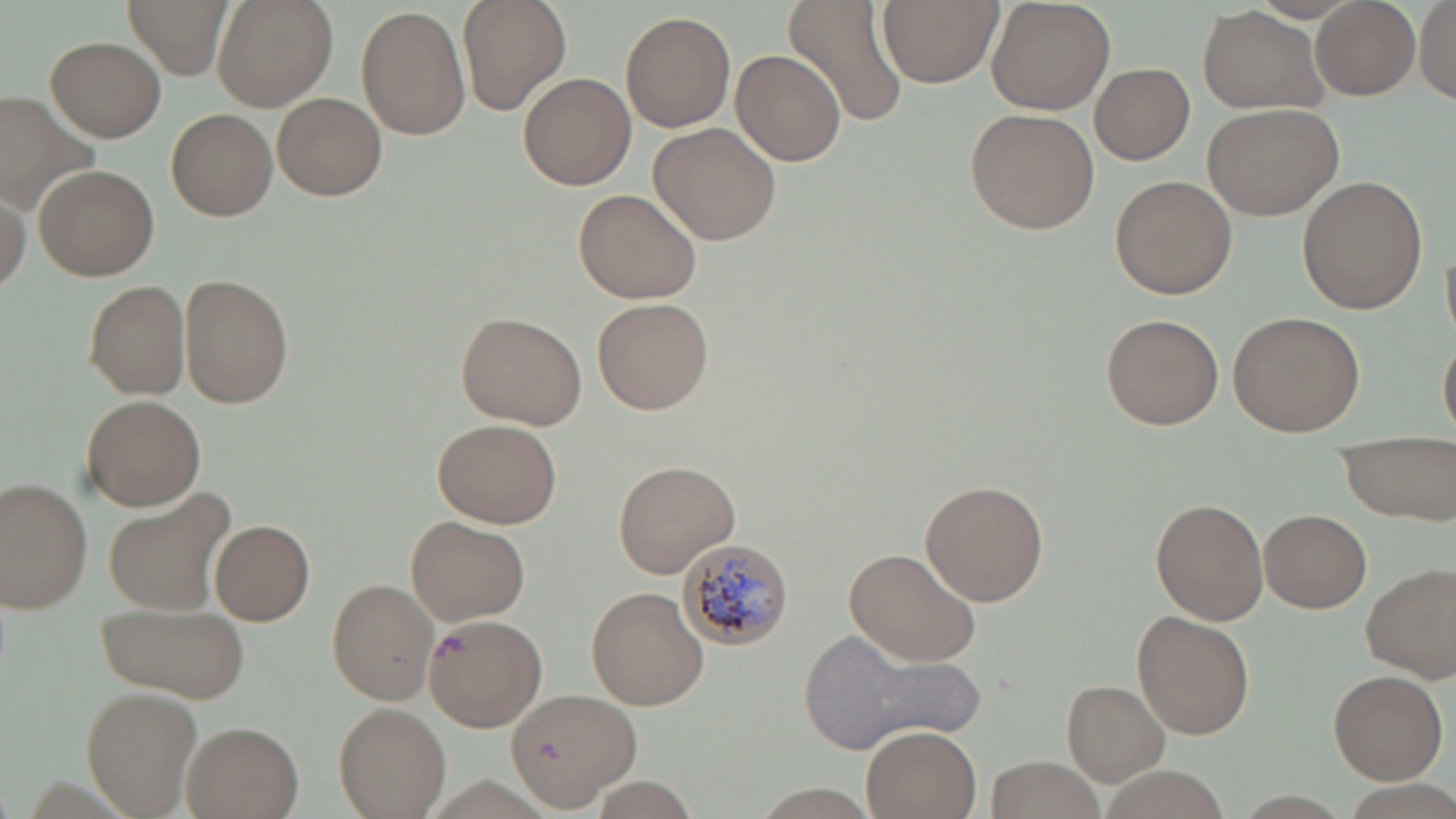 Approximate bounding boxes as (x1, y1, x2, y2) in pixels. Plasmodium malariae-infected red blood cell locations: (679, 538, 795, 651). Uninfected red blood cell locations: (123, 0, 234, 79), (456, 0, 571, 113), (784, 0, 911, 129), (877, 0, 1002, 89), (1312, 0, 1420, 100), (1416, 0, 1456, 107), (213, 1, 338, 111), (986, 2, 1116, 115), (355, 6, 470, 138), (1196, 6, 1329, 116), (620, 10, 736, 133), (46, 36, 165, 142), (731, 49, 848, 166), (1088, 64, 1194, 165), (517, 71, 636, 190), (0, 89, 101, 210), (274, 92, 386, 201), (1200, 102, 1344, 222), (964, 107, 1099, 235), (166, 108, 279, 221), (650, 123, 781, 245), (31, 163, 159, 282), (1110, 175, 1238, 299), (1295, 176, 1427, 314), (0, 185, 29, 295), (572, 187, 704, 304), (178, 274, 292, 408), (84, 279, 190, 400), (592, 297, 715, 414), (1228, 310, 1365, 436), (453, 311, 587, 429), (1099, 313, 1225, 430), (1437, 327, 1456, 442), (81, 395, 205, 511), (432, 417, 563, 529), (1335, 430, 1454, 523), (613, 460, 741, 578), (1, 478, 95, 613), (920, 479, 1050, 607), (104, 488, 237, 617), (1150, 499, 1268, 625), (1260, 509, 1371, 613), (405, 515, 530, 625), (209, 517, 315, 625), (843, 547, 984, 667), (1362, 563, 1456, 682), (327, 578, 439, 705), (586, 586, 707, 711), (94, 600, 248, 704), (1131, 610, 1255, 739), (424, 612, 548, 732), (803, 626, 982, 751), (1329, 669, 1447, 784), (1064, 680, 1172, 785), (79, 685, 203, 818), (504, 687, 641, 808), (335, 702, 449, 818), (180, 720, 305, 819), (858, 723, 984, 819), (984, 755, 1105, 818), (588, 779, 701, 815), (748, 784, 883, 816). Slide-level diagnosis: Plasmodium malariae. May-Grünwald-Giemsa stain. 1000x magnification. Light microscopy. One field of a larger specimen. Image is 1456×819 pixels. Thin blood film.